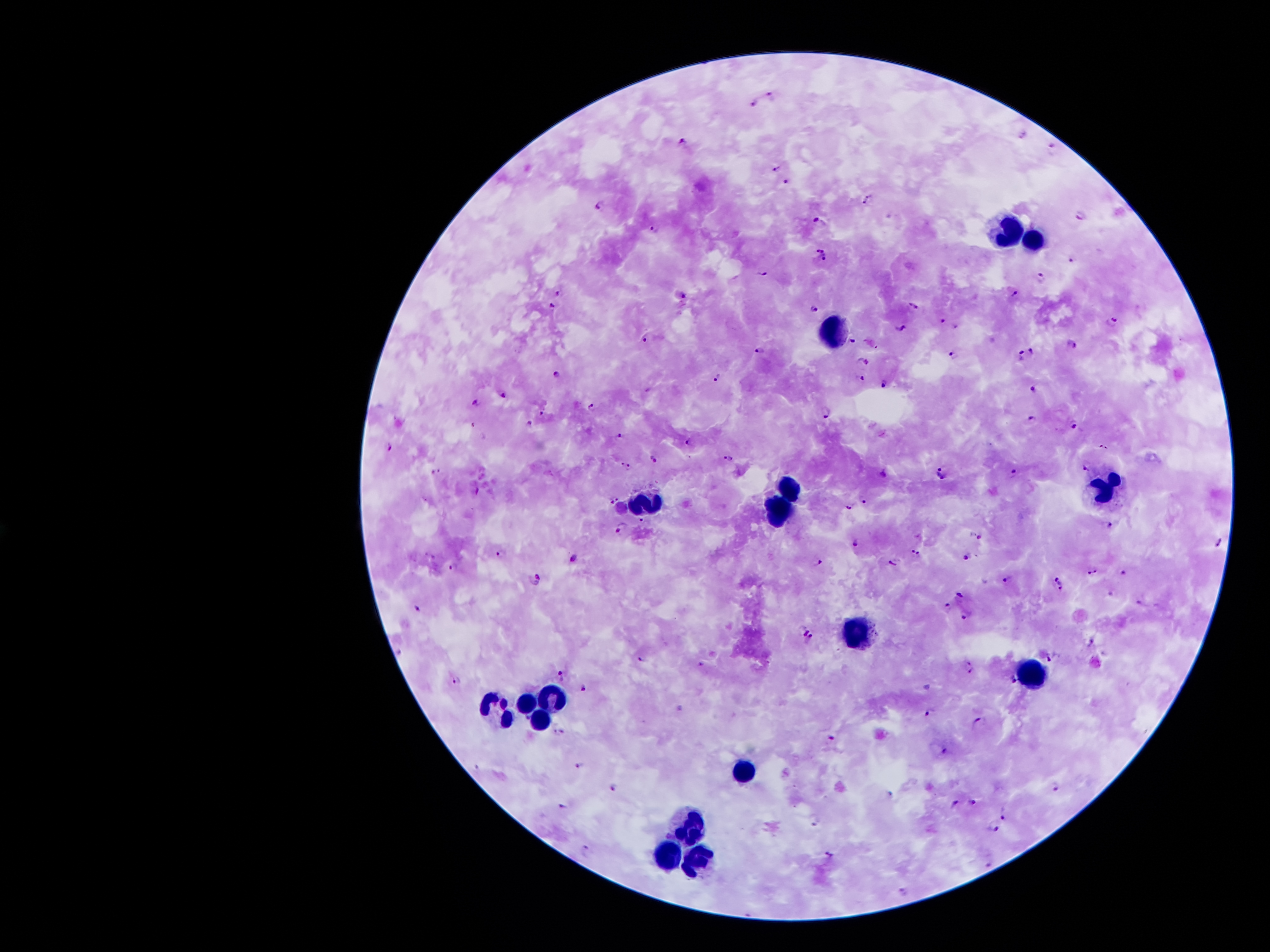 Approximate centers as (x, y) in pixels. Malaria parasite locations: (767, 95), (753, 103), (1023, 135), (683, 138), (1052, 149), (774, 169), (785, 180), (864, 203), (596, 206), (1080, 217), (815, 221), (653, 227), (822, 258), (1070, 258), (764, 273), (1042, 278), (559, 293), (1017, 295), (685, 296), (551, 306), (914, 306), (812, 307), (941, 320), (1114, 320), (900, 327), (853, 340), (644, 341), (1069, 343), (755, 350), (1030, 351), (948, 352), (1018, 354), (865, 361), (557, 374), (860, 378), (715, 381), (885, 384), (1030, 389), (503, 394), (477, 402), (592, 405), (542, 414), (824, 416), (1030, 417), (530, 422), (1072, 428), (621, 434), (689, 439), (389, 446), (729, 457), (654, 458), (622, 463), (629, 467), (1083, 469), (437, 472), (940, 472), (883, 474), (1012, 474), (478, 491), (614, 501), (849, 508), (642, 520), (1109, 524), (621, 526), (976, 535), (1221, 541), (854, 544), (915, 550), (499, 554), (966, 558), (573, 559), (893, 559), (820, 563), (455, 568), (1124, 572), (1093, 573), (539, 581), (1056, 581), (1007, 583), (960, 594), (1139, 603), (949, 607), (418, 610), (963, 618), (804, 629), (811, 641), (1093, 643), (1050, 659), (641, 660), (970, 660), (701, 664), (972, 672), (564, 676), (1013, 679), (457, 681), (582, 688), (929, 713), (977, 722), (558, 732), (830, 738), (943, 752), (579, 764), (1055, 787), (615, 788), (974, 802), (954, 804), (565, 807), (1005, 817), (813, 822), (995, 830), (584, 850), (829, 853), (992, 863), (905, 893). Leukocyte locations: (1008, 227), (1033, 241), (837, 333), (787, 482), (1108, 488), (646, 499), (776, 515), (857, 633), (1038, 679), (557, 693), (526, 700), (492, 709), (541, 718), (747, 773), (689, 826), (667, 854), (697, 858). Image is 1270×952 pixels. Giemsa stain. Smartphone photograph taken through the microscope eyepiece. Patient malaria status: infected with Plasmodium falciparum. Thick peripheral-blood smear. 100x magnification. Single field of view.